State which parasite is depicted.
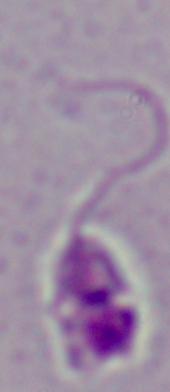

Leishmania.

Summary:
  - Magnification: 1000x
  - Modality: micrograph